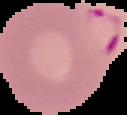

image type = segmented cell region with the area outside set to black
preparation = thin blood film
malaria status = parasitized
image size = 127×115 pixels